Locate and identify every blood parasite.
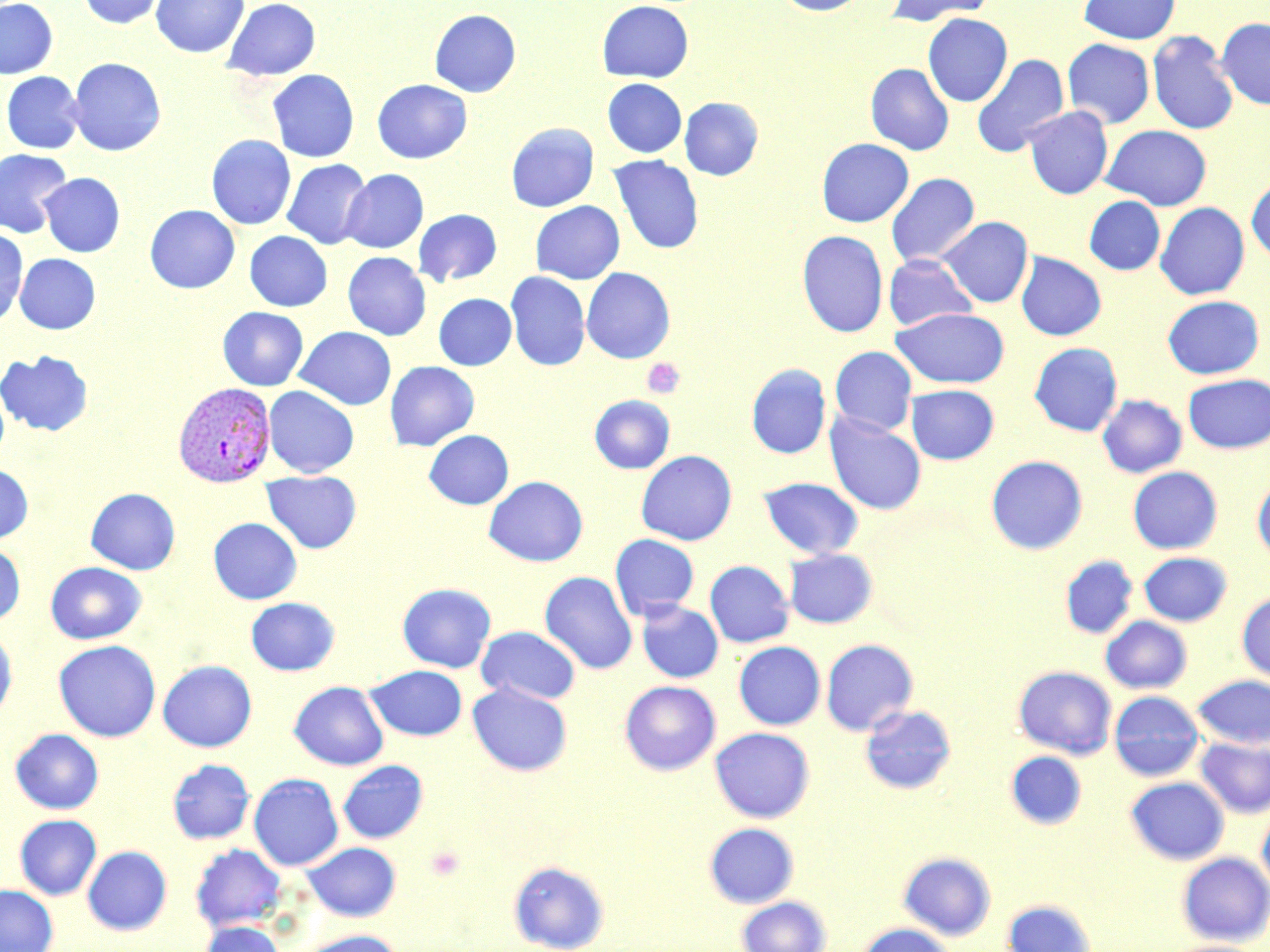
Approximate bounding boxes as (x1, y1, x2, y2) in pixels.
Plasmodium vivax-infected red blood cells: (173, 382, 276, 488).
No Plasmodium falciparum, Plasmodium ovale, Plasmodium malariae, Babesia divergens, or Trypanosoma brucei observed.

Platelet locations: (643, 358, 685, 399), (425, 844, 466, 882). Uninfected red blood cell locations: (0, 0, 58, 80), (77, 0, 166, 29), (151, 0, 249, 58), (223, 0, 321, 81), (774, 0, 868, 16), (884, 0, 997, 26), (1078, 0, 1181, 44), (597, 1, 693, 83), (429, 9, 521, 97), (922, 13, 1012, 107), (1217, 18, 1270, 109), (1147, 30, 1239, 135), (1062, 38, 1155, 129), (971, 54, 1069, 157), (67, 58, 166, 156), (865, 63, 954, 155), (267, 69, 359, 162), (2, 72, 85, 154), (602, 78, 687, 157), (372, 79, 472, 164), (679, 97, 764, 181), (1024, 106, 1113, 199), (506, 122, 599, 212), (1101, 124, 1212, 210), (206, 135, 296, 230), (816, 138, 914, 227), (0, 149, 72, 238), (609, 155, 704, 254), (282, 159, 372, 249), (340, 169, 428, 253), (39, 173, 125, 257), (885, 173, 980, 267), (1246, 175, 1270, 263), (1084, 196, 1165, 274), (530, 201, 624, 284), (1156, 202, 1250, 299), (145, 204, 240, 294), (413, 209, 502, 286), (937, 216, 1033, 308), (0, 227, 28, 326), (797, 230, 889, 337), (245, 231, 332, 311), (343, 252, 431, 340), (1016, 252, 1106, 341), (1023, 252, 1112, 437), (14, 253, 100, 334), (883, 254, 978, 331), (581, 267, 675, 363), (505, 271, 590, 370), (433, 293, 516, 370), (1162, 295, 1265, 379), (217, 307, 308, 391), (891, 307, 1009, 388), (295, 326, 396, 410), (1029, 342, 1123, 436), (829, 346, 917, 435), (0, 350, 93, 436), (385, 361, 479, 451), (745, 363, 831, 459), (1183, 374, 1270, 453), (0, 382, 9, 465), (906, 384, 999, 465), (264, 386, 359, 478), (589, 394, 675, 473), (1098, 394, 1187, 478), (825, 412, 926, 515), (424, 430, 513, 509), (636, 450, 737, 545), (986, 455, 1088, 555), (0, 463, 33, 543), (1128, 467, 1222, 554), (261, 470, 361, 553), (484, 476, 588, 566), (758, 476, 863, 559), (1252, 477, 1270, 563), (85, 488, 180, 574), (208, 517, 302, 604), (610, 534, 699, 619), (0, 541, 25, 626), (784, 548, 877, 629), (1138, 552, 1233, 626), (1060, 555, 1138, 639), (705, 560, 794, 647), (45, 561, 147, 644), (540, 571, 637, 674), (397, 583, 496, 673), (1237, 592, 1270, 684), (245, 597, 340, 675), (636, 600, 723, 683), (1100, 616, 1192, 693), (476, 626, 580, 705), (0, 629, 17, 721), (820, 638, 918, 736), (53, 640, 161, 742), (734, 641, 825, 730), (157, 660, 257, 752), (365, 665, 467, 740), (1012, 665, 1117, 759), (1192, 674, 1270, 749), (289, 680, 388, 770), (620, 680, 721, 775), (467, 681, 572, 776), (1109, 691, 1205, 781), (860, 704, 956, 794), (709, 727, 815, 823), (10, 728, 104, 814), (1195, 736, 1270, 818), (1005, 750, 1086, 829), (167, 758, 255, 844), (337, 760, 428, 843), (249, 773, 343, 870), (1125, 776, 1229, 864), (1257, 805, 1270, 895), (14, 814, 102, 900), (704, 822, 799, 908), (302, 841, 401, 921), (190, 844, 287, 932), (82, 845, 172, 935), (898, 852, 996, 940), (1177, 852, 1270, 945), (508, 860, 610, 952), (0, 885, 58, 952), (735, 896, 832, 952), (1002, 899, 1096, 952), (197, 920, 286, 952), (857, 923, 957, 952), (293, 929, 404, 952), (1160, 939, 1265, 952). Slide-level diagnosis: Plasmodium vivax. Thin blood film. Light microscopy. Single field of view. May-Grünwald-Giemsa-stained preparation. Image is 1270×952 pixels. 1000x magnification.